Assess this cell for malaria.
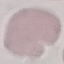

It is uninfected.

Summary:
  - Image type: automatically extracted cell patch, resized to 64 × 64 pixels
  - Capture: smartphone camera at the microscope eyepiece
  - Stain: Giemsa
  - Preparation: thin blood film